Point out each Plasmodium parasite.
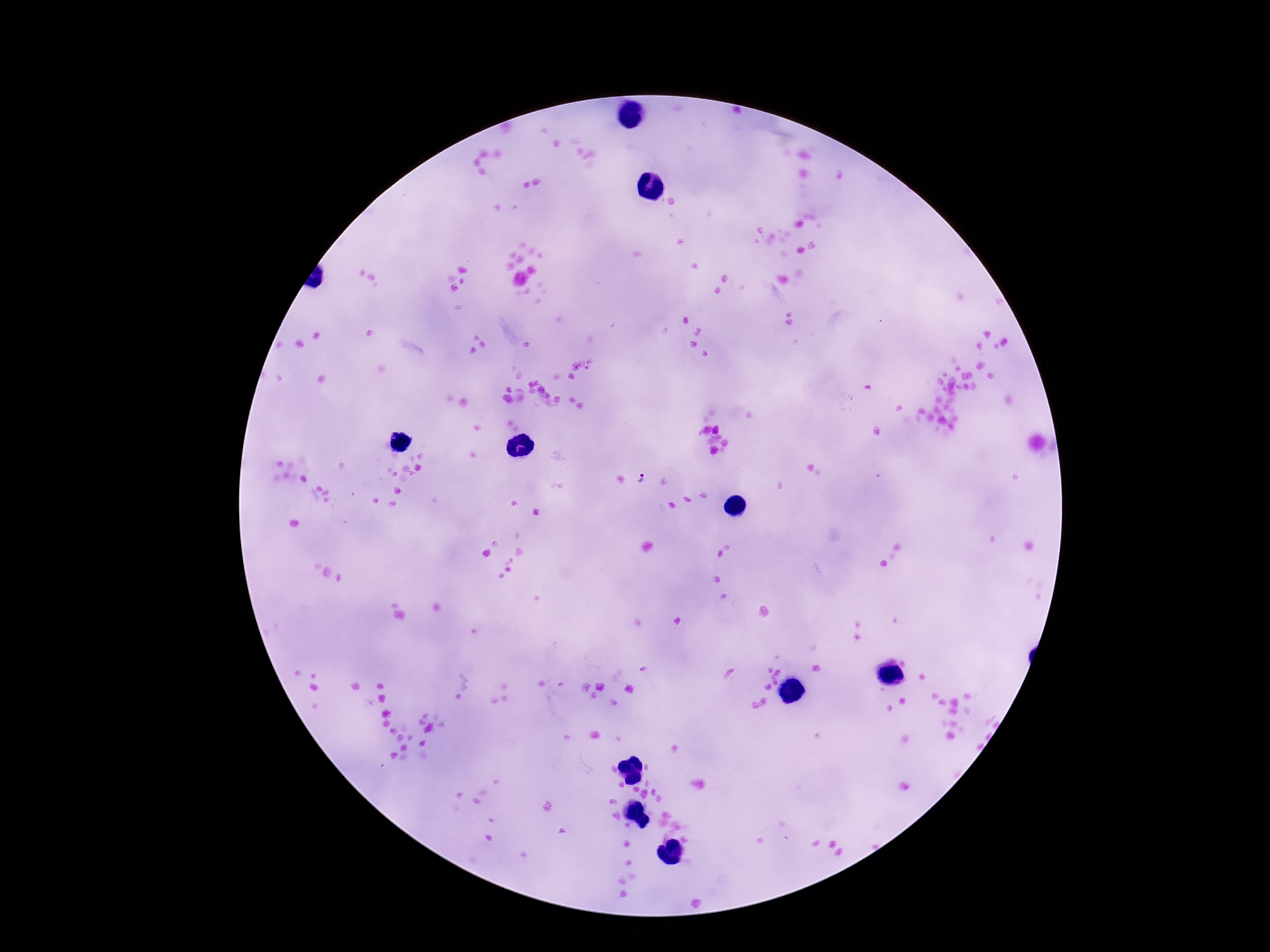

Approximate centers as (x, y) in pixels.
Plasmodium parasites: (640, 478).

Single field of view. Patient malaria status: infected. Thick blood film. Smartphone photograph taken through the microscope eyepiece. Image is 1270×952 pixels. Giemsa stain. 100x magnification.